Classify this cell by malaria status.
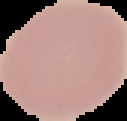
Uninfected.

Summary:
  - Preparation: thin blood film
  - Image size: 127×121 pixels
  - Image type: cell region segmented out of the field of view; surrounding area masked to black